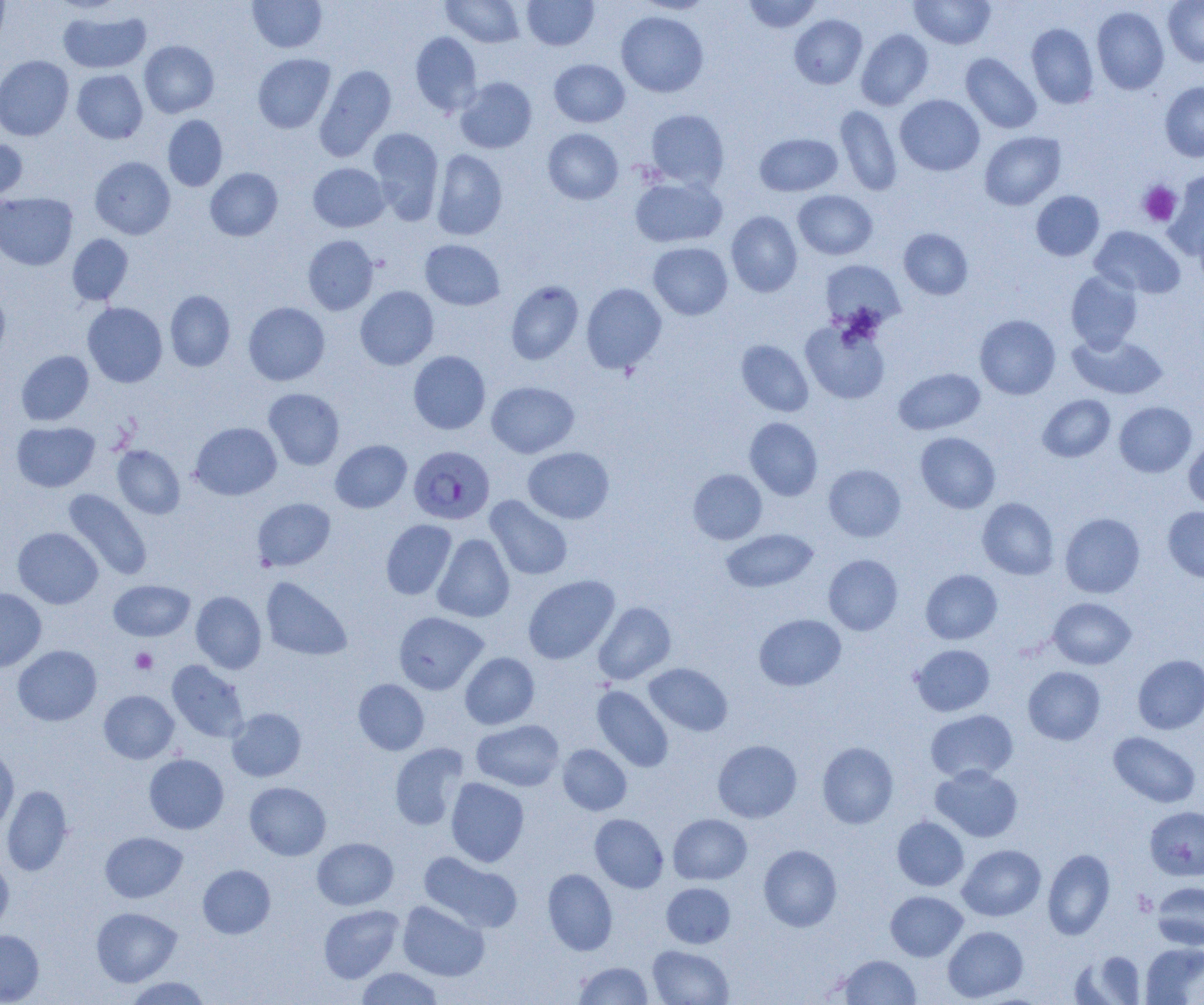
Summary:
  - Coordinate format: approximate bounding boxes as [x1, y1, x2, y2] in pixels
  - Plasmodium falciparum-infected red blood cell locations: [409, 445, 496, 525]
  - Platelet locations: [1138, 181, 1182, 227], [131, 648, 157, 674]
  - Uninfected red blood cell locations: [0, 0, 10, 48], [247, 0, 327, 53], [441, 0, 525, 47], [522, 0, 599, 50], [742, 0, 822, 33], [909, 0, 996, 49], [1163, 0, 1204, 66], [636, 1, 715, 14], [1092, 6, 1169, 94], [58, 8, 151, 74], [616, 11, 709, 97], [789, 14, 867, 88], [1026, 23, 1099, 109], [856, 29, 934, 110], [410, 31, 482, 116], [139, 40, 219, 118], [252, 53, 335, 133], [961, 53, 1042, 134], [0, 56, 74, 141], [549, 59, 630, 127], [315, 65, 396, 161], [72, 70, 148, 143], [455, 77, 537, 153], [1160, 81, 1204, 161], [895, 95, 985, 176], [835, 105, 902, 196], [645, 109, 729, 189], [162, 115, 228, 191], [368, 128, 444, 224], [543, 128, 623, 204], [979, 131, 1066, 210], [755, 133, 842, 196], [0, 138, 28, 203], [432, 149, 507, 240], [90, 156, 175, 239], [308, 163, 390, 232], [205, 168, 282, 241], [1163, 173, 1204, 260], [629, 176, 727, 248], [793, 190, 877, 260], [1031, 191, 1105, 261], [0, 192, 78, 270], [725, 211, 802, 297], [1089, 226, 1185, 298], [899, 228, 973, 300], [67, 234, 133, 305], [303, 235, 379, 315], [420, 239, 505, 310], [648, 242, 733, 319], [820, 259, 905, 331], [1065, 270, 1143, 353], [506, 280, 584, 365], [581, 283, 667, 374], [355, 286, 439, 370], [0, 288, 11, 366], [165, 290, 235, 372], [82, 302, 167, 387], [243, 302, 329, 385], [975, 314, 1060, 399], [800, 318, 890, 404], [1067, 332, 1168, 400], [736, 340, 814, 417], [16, 351, 93, 425], [408, 351, 490, 434], [893, 368, 985, 435], [486, 381, 579, 458], [263, 388, 345, 470], [1037, 394, 1115, 462], [1114, 401, 1197, 477], [744, 417, 823, 500], [12, 421, 100, 492], [190, 422, 281, 500], [915, 432, 1000, 513], [1184, 437, 1204, 510], [330, 440, 411, 512], [112, 445, 185, 519], [523, 447, 614, 523], [823, 464, 906, 542], [688, 469, 767, 544], [63, 488, 152, 581], [485, 495, 572, 580], [252, 497, 335, 571], [255, 497, 337, 655], [977, 497, 1059, 580], [1163, 506, 1204, 582], [1059, 512, 1145, 598], [381, 519, 457, 600], [13, 527, 103, 608], [721, 529, 818, 592], [433, 534, 514, 622], [823, 555, 903, 635], [921, 569, 1002, 644], [523, 574, 620, 664], [261, 577, 352, 661], [109, 580, 195, 641], [0, 588, 47, 672], [191, 591, 266, 674], [1048, 597, 1136, 669], [593, 601, 676, 684], [393, 611, 488, 694], [754, 614, 846, 691], [910, 644, 995, 716], [13, 645, 101, 725], [460, 652, 540, 729], [1132, 654, 1204, 734], [167, 660, 249, 743], [643, 663, 733, 736], [1023, 666, 1105, 745], [353, 679, 429, 755], [592, 685, 673, 772], [99, 690, 179, 764], [227, 708, 306, 781], [925, 709, 1018, 783], [471, 719, 564, 791], [1108, 731, 1201, 808], [713, 739, 802, 822], [817, 741, 898, 828], [390, 743, 468, 830], [558, 744, 632, 815], [0, 747, 19, 835], [144, 753, 229, 834], [930, 764, 1023, 842], [446, 778, 529, 866], [244, 782, 331, 860], [2, 785, 73, 876], [1144, 806, 1204, 880], [589, 813, 669, 892], [668, 814, 752, 884], [892, 816, 969, 891], [100, 831, 187, 903], [312, 837, 398, 910], [758, 844, 842, 931], [957, 844, 1046, 921], [1042, 848, 1115, 940], [418, 851, 522, 933], [0, 857, 14, 935], [198, 864, 276, 939], [543, 868, 618, 955], [1152, 881, 1204, 950], [661, 882, 735, 948], [885, 891, 967, 961], [397, 900, 489, 981], [318, 904, 404, 983], [91, 907, 182, 986], [943, 925, 1028, 1002], [0, 930, 44, 1004], [1141, 942, 1204, 1004], [647, 944, 733, 1005], [1073, 951, 1146, 1004], [837, 954, 921, 1004], [573, 961, 653, 1004], [356, 967, 444, 1004], [124, 976, 211, 1004]
  - Slide-level diagnosis: Plasmodium falciparum
  - Modality: optical microscopy
  - Field of view: one of a larger specimen
  - Preparation: thin blood smear
  - Magnification: 1000x
  - Image size: 1204×1005 pixels